Locate every uninfected red blood cell.
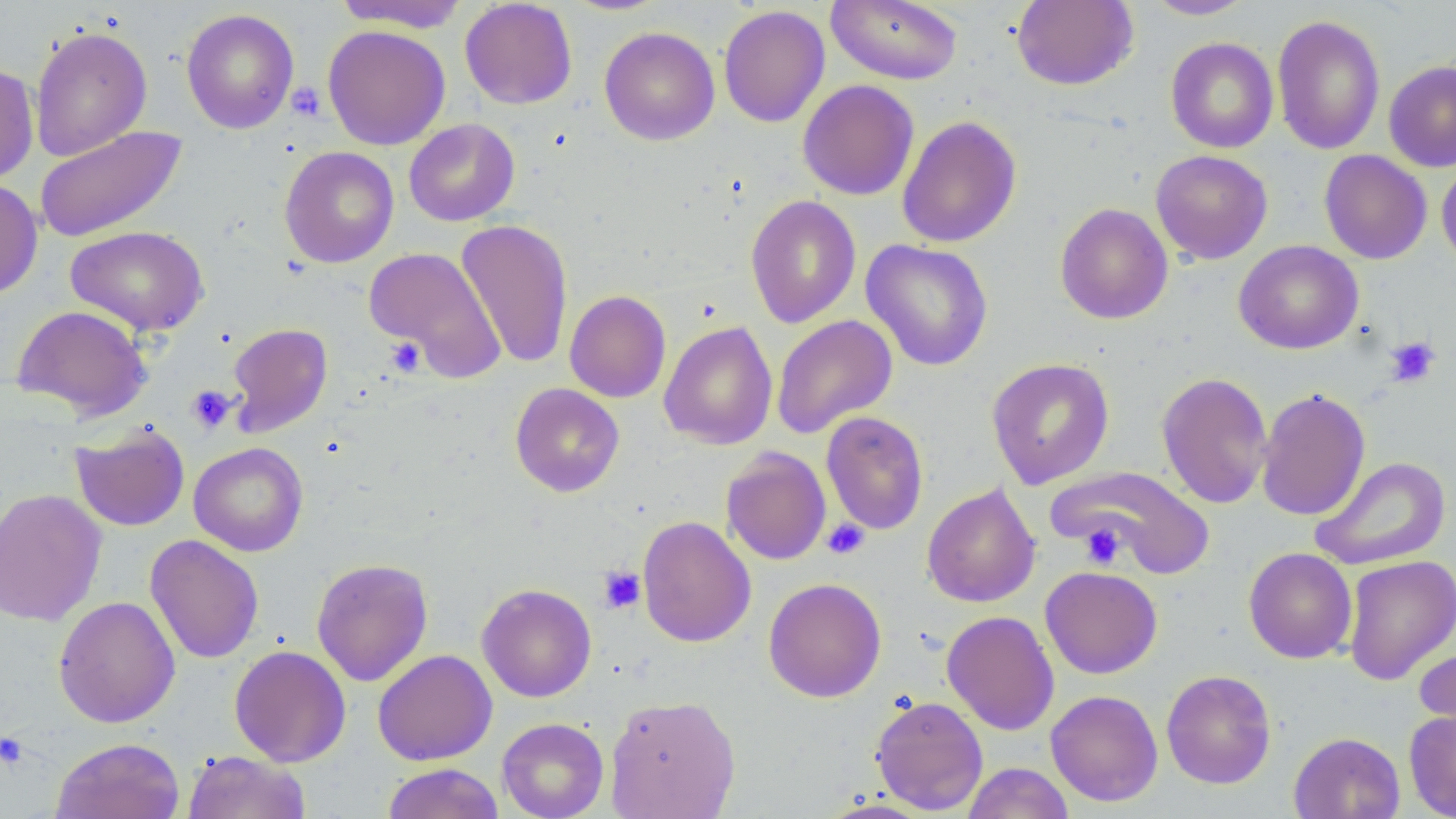

Approximate bounding boxes as (x1,y1)-(x2,y2) corner pairs in pixels.
Uninfected red blood cells: (459,0)-(577,109), (826,0)-(962,85), (1012,0)-(1139,90), (1143,0)-(1257,20), (333,1)-(469,32), (718,4)-(830,128), (180,8)-(299,134), (1272,14)-(1386,155), (29,25)-(153,161), (323,25)-(451,150), (599,26)-(720,146), (1165,37)-(1279,153), (1384,60)-(1456,172), (0,63)-(39,186), (797,79)-(919,200), (897,115)-(1022,248), (404,118)-(520,226), (33,126)-(188,243), (280,146)-(399,267), (1151,149)-(1273,264), (1319,149)-(1432,264), (1436,158)-(1456,270), (0,179)-(43,299), (745,194)-(861,329), (1055,202)-(1173,324), (455,220)-(574,369), (66,225)-(209,337), (861,240)-(994,371), (1234,240)-(1363,354), (364,247)-(505,380), (564,290)-(671,403), (11,304)-(152,420), (772,314)-(897,439), (659,321)-(778,450), (227,322)-(333,437), (986,357)-(1115,490), (1156,371)-(1273,510), (510,383)-(625,497), (1256,387)-(1371,521), (821,411)-(929,534), (70,423)-(190,532), (189,442)-(308,556), (721,447)-(831,565), (1310,456)-(1451,570), (1053,466)-(1215,579), (921,483)-(1041,608), (0,488)-(107,627), (637,516)-(756,647), (145,535)-(264,663), (1243,547)-(1357,664), (1342,554)-(1456,686), (311,557)-(434,687), (1040,566)-(1163,679), (763,577)-(887,703), (476,583)-(597,702), (53,596)-(180,727), (941,610)-(1060,735), (229,645)-(351,767), (1414,645)-(1456,744), (373,649)-(497,765), (1161,669)-(1276,789), (1046,689)-(1163,806), (605,694)-(741,818), (870,695)-(989,814), (1403,711)-(1456,818), (497,717)-(610,819), (1289,731)-(1405,819), (51,737)-(186,819), (183,750)-(312,819), (961,762)-(1074,819), (380,763)-(505,819), (815,799)-(940,818).

slide-level diagnosis = negative for blood parasites
platelet locations = approximate bounding boxes as (x1,y1)-(x2,y2) corner pairs in pixels: (287,81)-(326,121), (1384,336)-(1441,388), (384,337)-(425,378), (185,385)-(237,434), (821,519)-(870,559), (1080,523)-(1125,568), (598,566)-(646,614), (0,731)-(31,770)
modality = light microscopy
stain = May-Grünwald-Giemsa
image size = 1456×819 pixels
field of view = one of a larger specimen
preparation = thin blood smear
magnification = 1000x